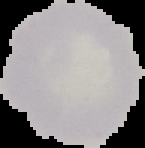
The area outside the segmented cell region is set to black. From a thin blood film. Malaria status: uninfected. Image is 145×148 pixels.